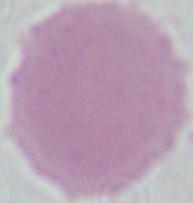
Summary:
  - Identification: erythrocyte
  - Modality: photomicrograph
  - Magnification: 1000x